Give the position of every Plasmodium parasite.
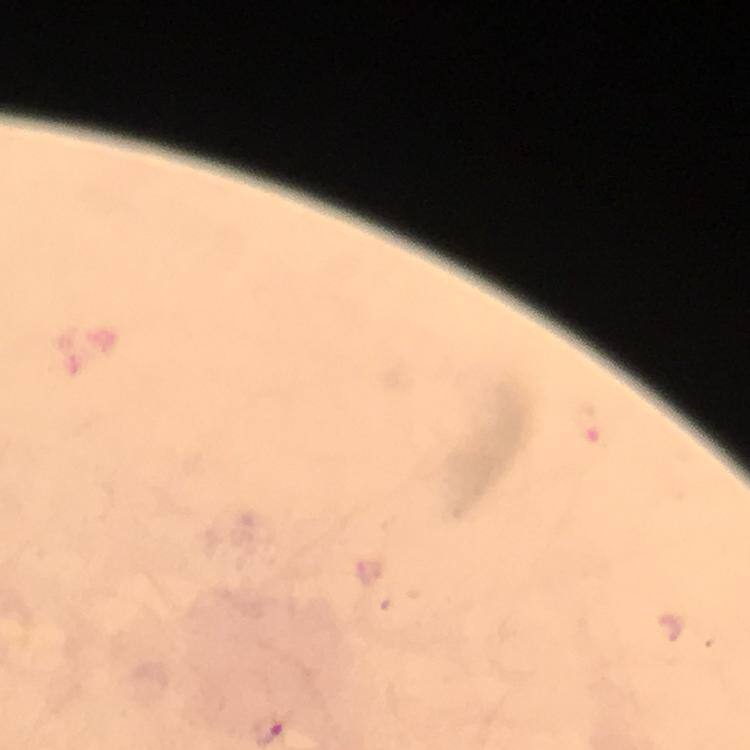

Approximate centers as (x, y) in pixels.
Plasmodium parasites: (588, 424).

Summary:
  - Stain: Giemsa
  - Cropped from: a single field of view
  - Context: from a diagnostic examination for malaria
  - Capture: smartphone mounted on the microscope
  - Magnification: 100x
  - Preparation: thick blood smear
  - Image size: 750×750 pixels
  - Immersion oil: used